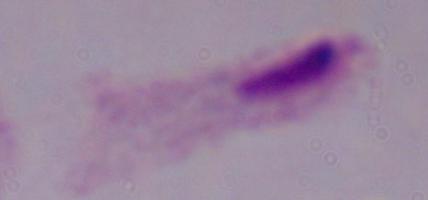 Micrograph. 1000x magnification. A trichomonad is shown.